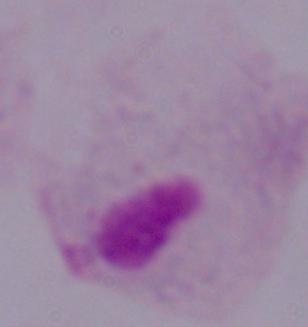

magnification = 1000x
modality = photomicrograph
identification = trichomonad